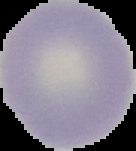
image_size: 136×151 pixels
preparation: thin blood smear
image_type: segmented cell region with the area outside set to black
result: no malaria parasites seen